Comment on the morphology of the erythrocytes.
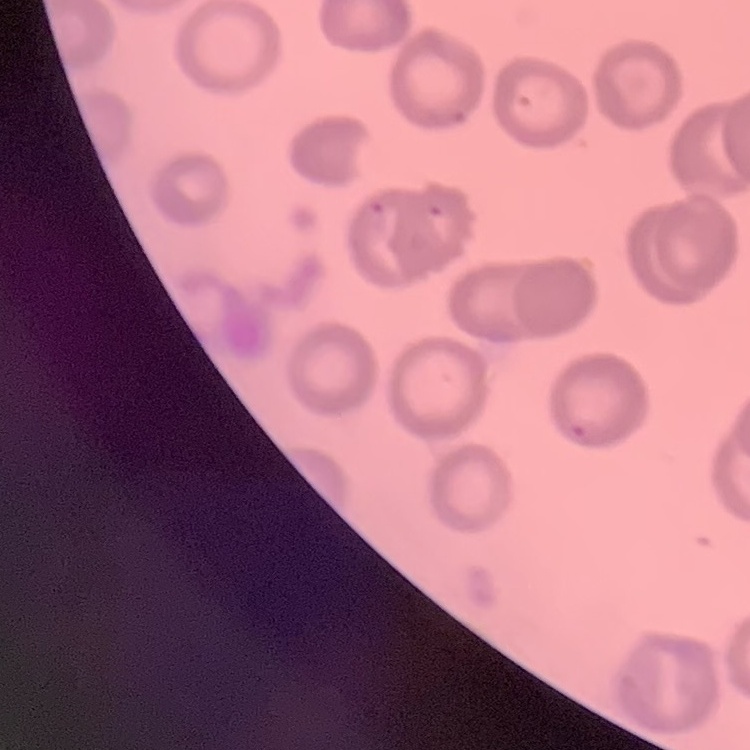
No rouleaux formation.

Summary:
  - Image type: square crop of a larger photomicrograph
  - Stain: Field's or Giemsa
  - Preparation: thin peripheral smear